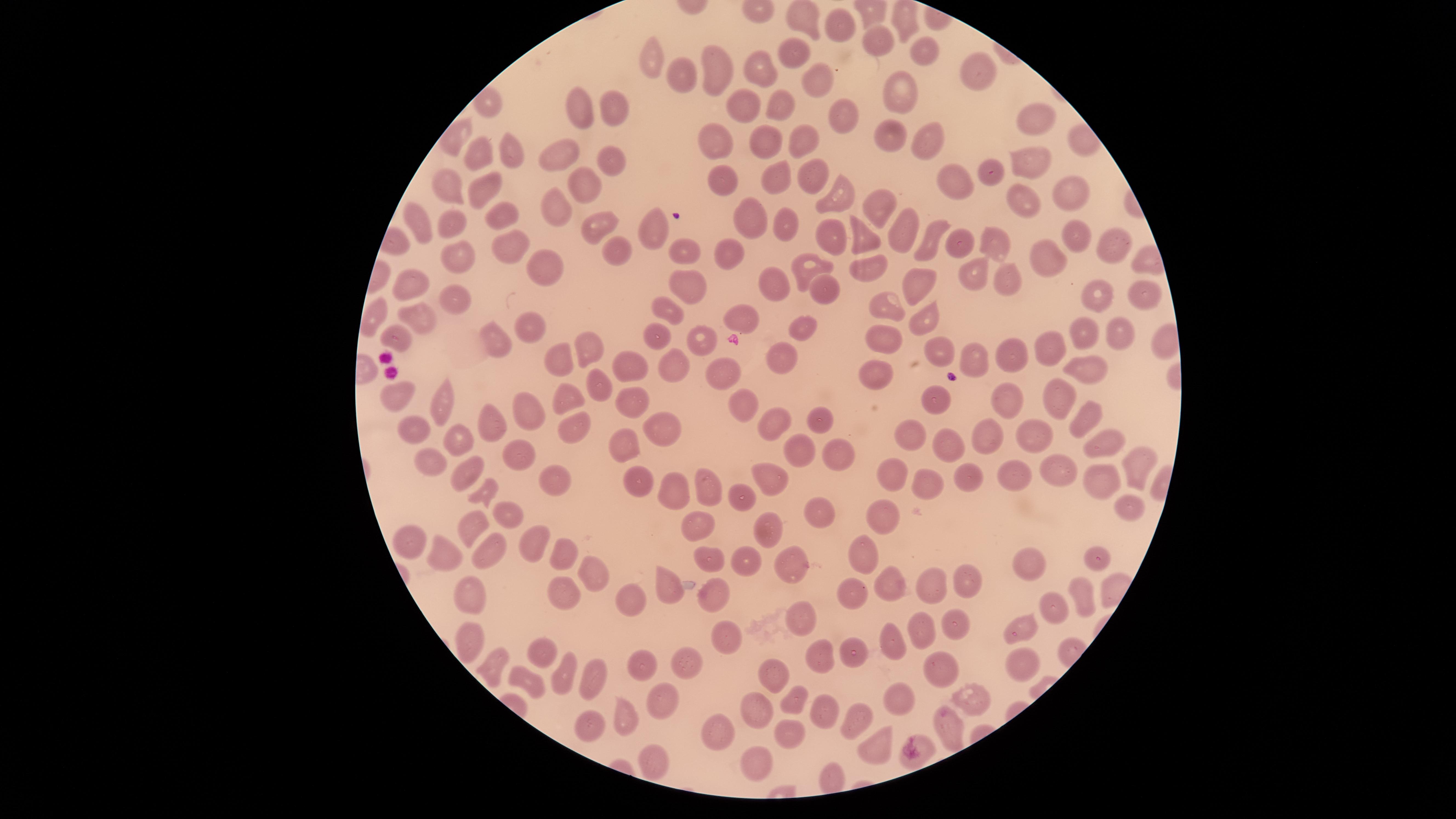

Approximate marker points, in pixels from the top-left corner.
Summary:
  - Uninfected red blood cells: (x=808, y=15), (x=839, y=29), (x=876, y=39), (x=922, y=46), (x=790, y=52), (x=657, y=55), (x=757, y=63), (x=714, y=68), (x=977, y=69), (x=678, y=75), (x=815, y=79), (x=900, y=91), (x=484, y=101), (x=579, y=102), (x=743, y=106), (x=616, y=107), (x=782, y=109), (x=843, y=115), (x=1033, y=116), (x=794, y=132), (x=893, y=137), (x=922, y=137), (x=767, y=140), (x=715, y=143), (x=477, y=149), (x=512, y=153), (x=558, y=154), (x=1028, y=159), (x=612, y=161), (x=727, y=175), (x=811, y=175), (x=996, y=175), (x=960, y=177), (x=779, y=178), (x=587, y=182), (x=445, y=184), (x=483, y=185), (x=1073, y=190), (x=832, y=192), (x=1020, y=199), (x=878, y=200), (x=557, y=204), (x=503, y=208), (x=418, y=215), (x=750, y=216), (x=778, y=218), (x=451, y=222), (x=597, y=226), (x=661, y=227), (x=905, y=228), (x=828, y=229), (x=860, y=229), (x=1075, y=236), (x=929, y=238), (x=994, y=240), (x=620, y=243), (x=516, y=244), (x=1107, y=244), (x=962, y=245), (x=685, y=246), (x=452, y=250), (x=729, y=254), (x=1053, y=258), (x=869, y=262), (x=809, y=263), (x=534, y=265), (x=976, y=272), (x=682, y=273), (x=1010, y=278), (x=408, y=281), (x=919, y=281), (x=823, y=284), (x=771, y=285), (x=451, y=294), (x=1099, y=295), (x=1148, y=295), (x=670, y=302), (x=890, y=305), (x=373, y=311), (x=420, y=316), (x=744, y=316), (x=925, y=318), (x=524, y=324), (x=805, y=325), (x=1116, y=331), (x=1090, y=332), (x=399, y=334), (x=657, y=337), (x=699, y=337), (x=485, y=339), (x=882, y=340), (x=1039, y=340), (x=587, y=342), (x=936, y=347), (x=560, y=351), (x=1015, y=356), (x=978, y=357), (x=787, y=360), (x=872, y=362), (x=1090, y=365), (x=631, y=370), (x=678, y=370), (x=726, y=370), (x=404, y=392), (x=573, y=396), (x=628, y=397), (x=443, y=398), (x=740, y=399), (x=938, y=399), (x=1063, y=400), (x=1000, y=407), (x=526, y=412), (x=1085, y=415), (x=816, y=419), (x=485, y=420), (x=665, y=424), (x=776, y=424), (x=411, y=426), (x=573, y=426), (x=908, y=427), (x=1037, y=429), (x=448, y=434), (x=989, y=436), (x=951, y=438), (x=1104, y=440), (x=619, y=441), (x=802, y=446), (x=832, y=451), (x=1135, y=456), (x=521, y=457), (x=433, y=461), (x=896, y=467), (x=971, y=468), (x=1067, y=468), (x=636, y=470), (x=461, y=471), (x=762, y=473), (x=1014, y=473), (x=552, y=479), (x=933, y=480), (x=1104, y=480), (x=700, y=482), (x=484, y=484), (x=663, y=485), (x=740, y=488), (x=1127, y=504), (x=815, y=507), (x=887, y=509), (x=511, y=513), (x=701, y=516), (x=471, y=517), (x=762, y=523), (x=530, y=536), (x=487, y=540), (x=411, y=541), (x=557, y=548), (x=703, y=551), (x=865, y=551), (x=1098, y=551), (x=443, y=555), (x=792, y=559), (x=744, y=560), (x=1041, y=563), (x=592, y=565), (x=923, y=577), (x=672, y=580), (x=892, y=580), (x=961, y=581), (x=852, y=587), (x=726, y=590), (x=565, y=594), (x=1089, y=594), (x=635, y=596), (x=466, y=597), (x=1056, y=612), (x=798, y=613), (x=955, y=623), (x=923, y=625), (x=1023, y=626), (x=724, y=631), (x=892, y=639), (x=466, y=642), (x=539, y=650), (x=849, y=654), (x=816, y=655), (x=1019, y=659), (x=644, y=660), (x=690, y=660), (x=937, y=661), (x=492, y=665), (x=778, y=672), (x=564, y=673), (x=597, y=677), (x=528, y=678), (x=901, y=691), (x=967, y=692), (x=795, y=693), (x=658, y=695), (x=756, y=707), (x=616, y=712), (x=827, y=714), (x=860, y=715), (x=951, y=719), (x=589, y=721), (x=715, y=727), (x=792, y=734), (x=880, y=742), (x=646, y=752), (x=922, y=756), (x=751, y=759), (x=830, y=776)
  - Stain: Giemsa
  - Image size: 1456×819 pixels
  - Presence: no malaria parasites detected
  - Field of view: single
  - Capture: smartphone photograph through the microscope eyepiece
  - Preparation: thin blood smear
  - Visible region: circular